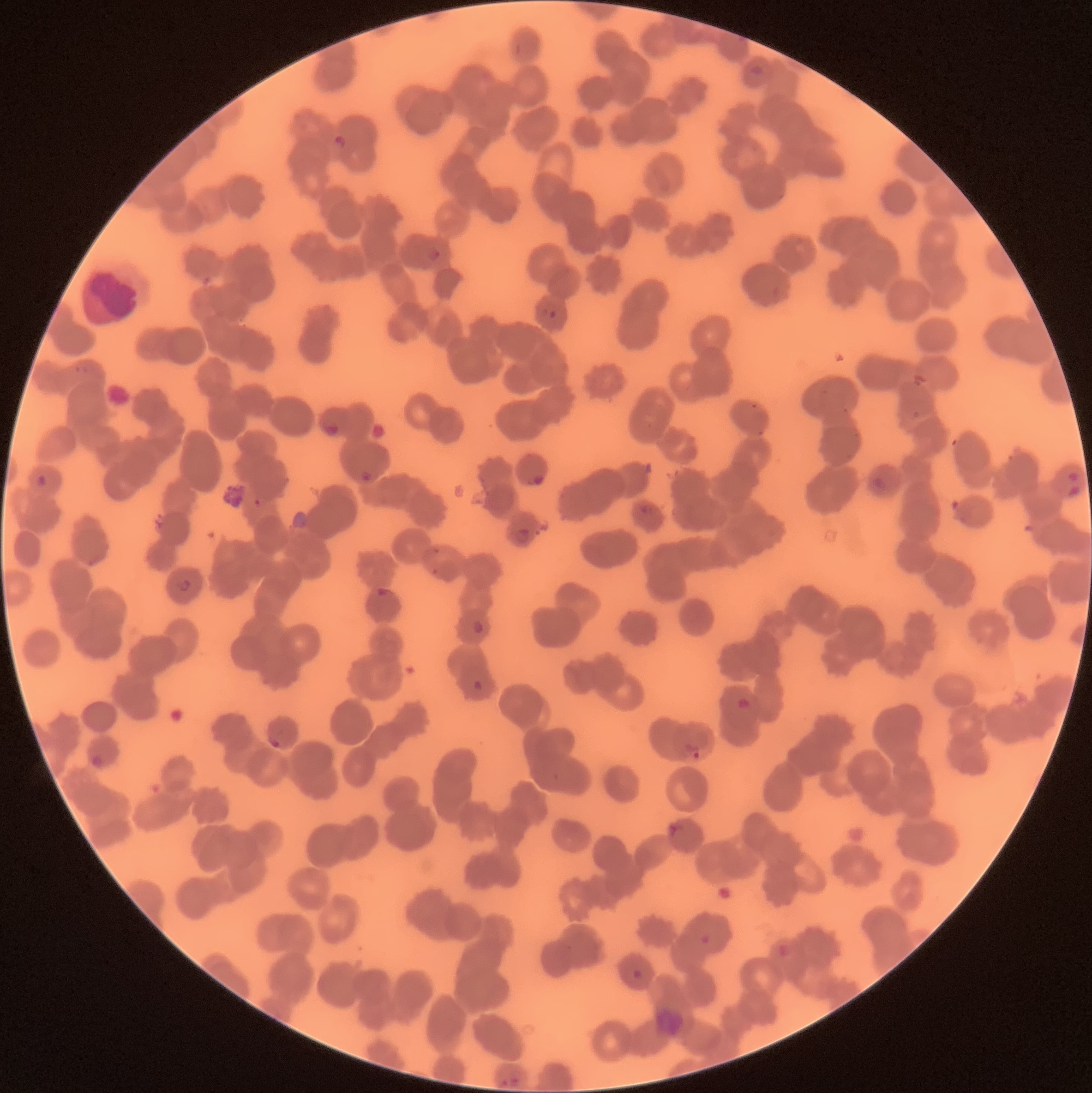
Summary:
  - Coordinate format: approximate bounding boxes as (x1,y1)-(x2,y2) corner pairs in pixels
  - Plasmodium parasite locations: (332,134)-(347,150), (425,245)-(441,261), (542,305)-(562,321), (324,421)-(340,439), (359,470)-(375,483), (1066,471)-(1081,482), (35,473)-(49,488), (526,473)-(544,488), (872,476)-(888,494), (1066,484)-(1081,498), (635,504)-(649,521), (515,526)-(531,545), (174,579)-(192,593), (374,587)-(390,597), (470,619)-(484,635), (471,680)-(483,692), (737,697)-(753,713), (268,736)-(281,749), (683,743)-(701,760), (90,754)-(102,771), (668,823)-(683,839), (700,933)-(711,946), (631,969)-(645,982), (501,1074)-(521,1088)
  - Modality: optical microscopy
  - Preparation: thin blood film
  - Image size: 1092×1093 pixels
  - Red blood cell morphology: rouleaux formation